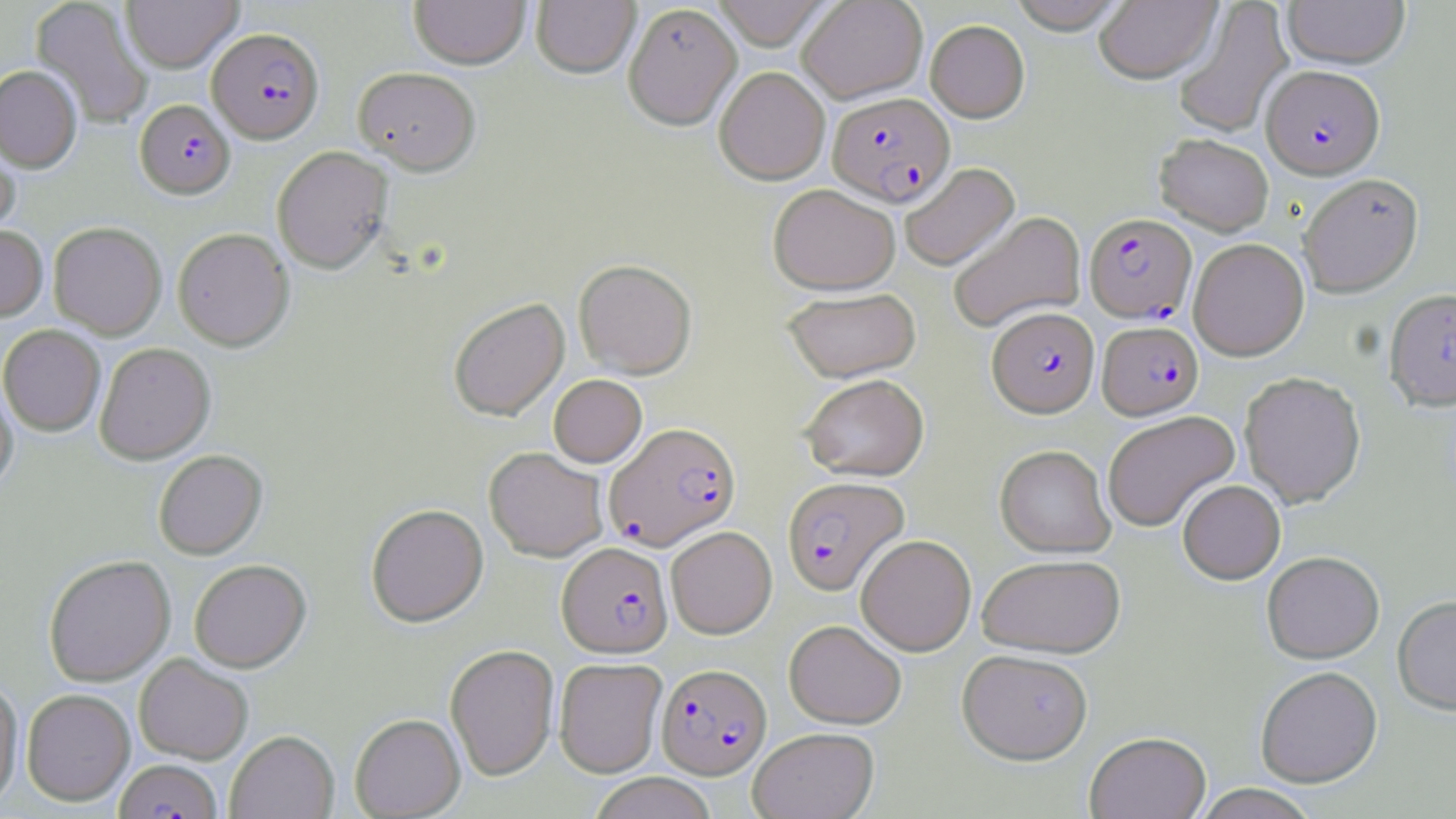 Approximate bounding boxes as named x1/y1/x2/y2 corners in pixels. Plasmodium falciparum-infected red blood cell locations: (x1=208, y1=27, x2=325, y2=143), (x1=1262, y1=64, x2=1384, y2=179), (x1=827, y1=92, x2=954, y2=206), (x1=135, y1=99, x2=235, y2=198), (x1=1084, y1=212, x2=1197, y2=323), (x1=988, y1=306, x2=1099, y2=416), (x1=1097, y1=320, x2=1203, y2=419), (x1=605, y1=422, x2=741, y2=551), (x1=782, y1=476, x2=908, y2=594), (x1=557, y1=542, x2=673, y2=658), (x1=656, y1=662, x2=771, y2=779), (x1=114, y1=758, x2=222, y2=819). Uninfected red blood cell locations: (x1=30, y1=0, x2=153, y2=128), (x1=120, y1=0, x2=242, y2=72), (x1=409, y1=0, x2=530, y2=69), (x1=531, y1=0, x2=641, y2=78), (x1=711, y1=0, x2=834, y2=49), (x1=797, y1=0, x2=928, y2=103), (x1=1007, y1=0, x2=1132, y2=33), (x1=1094, y1=1, x2=1221, y2=83), (x1=1173, y1=1, x2=1293, y2=138), (x1=1282, y1=1, x2=1410, y2=69), (x1=623, y1=2, x2=742, y2=130), (x1=925, y1=19, x2=1030, y2=122), (x1=0, y1=65, x2=82, y2=172), (x1=353, y1=66, x2=481, y2=175), (x1=714, y1=66, x2=830, y2=184), (x1=0, y1=121, x2=21, y2=240), (x1=1154, y1=133, x2=1274, y2=235), (x1=272, y1=146, x2=393, y2=273), (x1=899, y1=162, x2=1020, y2=271), (x1=1298, y1=173, x2=1423, y2=297), (x1=768, y1=183, x2=900, y2=294), (x1=948, y1=211, x2=1086, y2=333), (x1=48, y1=221, x2=166, y2=339), (x1=0, y1=224, x2=48, y2=321), (x1=172, y1=227, x2=294, y2=350), (x1=1188, y1=238, x2=1309, y2=361), (x1=573, y1=259, x2=697, y2=378), (x1=1384, y1=286, x2=1456, y2=411), (x1=783, y1=287, x2=921, y2=382), (x1=448, y1=297, x2=569, y2=421), (x1=0, y1=325, x2=105, y2=436), (x1=95, y1=342, x2=215, y2=464), (x1=1239, y1=370, x2=1366, y2=508), (x1=799, y1=373, x2=929, y2=481), (x1=548, y1=375, x2=647, y2=467), (x1=0, y1=379, x2=18, y2=495), (x1=1101, y1=410, x2=1240, y2=532), (x1=995, y1=445, x2=1115, y2=557), (x1=484, y1=447, x2=608, y2=561), (x1=154, y1=449, x2=267, y2=560), (x1=1178, y1=480, x2=1286, y2=584), (x1=366, y1=503, x2=489, y2=627), (x1=665, y1=526, x2=777, y2=638), (x1=856, y1=534, x2=976, y2=656), (x1=1262, y1=551, x2=1384, y2=663), (x1=43, y1=554, x2=176, y2=686), (x1=977, y1=554, x2=1125, y2=657), (x1=189, y1=560, x2=311, y2=672), (x1=1392, y1=595, x2=1456, y2=715), (x1=783, y1=619, x2=907, y2=728), (x1=445, y1=644, x2=559, y2=781), (x1=958, y1=648, x2=1093, y2=763), (x1=134, y1=654, x2=253, y2=764), (x1=554, y1=658, x2=667, y2=777), (x1=1255, y1=666, x2=1382, y2=787), (x1=0, y1=676, x2=23, y2=809), (x1=22, y1=688, x2=135, y2=805), (x1=350, y1=713, x2=465, y2=818), (x1=748, y1=727, x2=879, y2=819), (x1=225, y1=730, x2=339, y2=819), (x1=1084, y1=731, x2=1211, y2=819), (x1=587, y1=772, x2=718, y2=819), (x1=1192, y1=784, x2=1321, y2=819). Slide-level diagnosis: Plasmodium falciparum. Captured at 1000x magnification. Thin blood smear. Image is 1456×819 pixels. May-Grünwald-Giemsa stain. Optical microscopy. One field of a larger specimen.